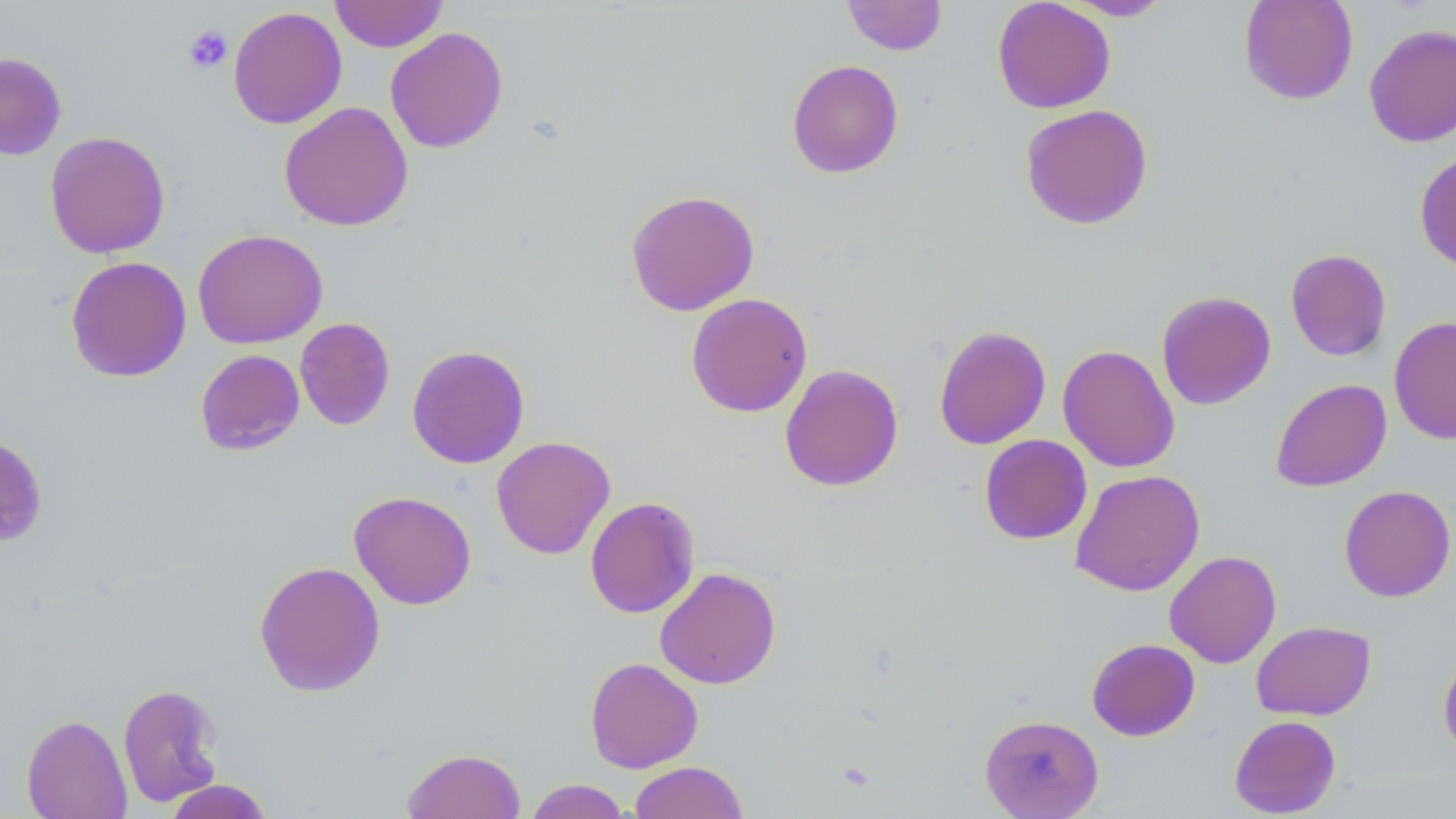

Approximate bounding boxes as named x1/y1/x2/y2 corners in pixels. Uninfected red blood cell locations: (x1=330, y1=0, x2=448, y2=52), (x1=842, y1=0, x2=947, y2=56), (x1=992, y1=0, x2=1115, y2=114), (x1=1062, y1=0, x2=1173, y2=21), (x1=1238, y1=0, x2=1359, y2=105), (x1=228, y1=6, x2=346, y2=130), (x1=1364, y1=23, x2=1456, y2=147), (x1=385, y1=27, x2=509, y2=154), (x1=0, y1=51, x2=66, y2=161), (x1=786, y1=59, x2=904, y2=179), (x1=279, y1=101, x2=413, y2=232), (x1=1020, y1=104, x2=1154, y2=230), (x1=45, y1=131, x2=170, y2=258), (x1=1414, y1=150, x2=1456, y2=272), (x1=625, y1=189, x2=760, y2=316), (x1=192, y1=229, x2=328, y2=348), (x1=1279, y1=248, x2=1390, y2=491), (x1=1285, y1=249, x2=1392, y2=361), (x1=65, y1=256, x2=191, y2=382), (x1=1156, y1=290, x2=1276, y2=410), (x1=686, y1=293, x2=813, y2=418), (x1=1389, y1=316, x2=1456, y2=444), (x1=295, y1=317, x2=395, y2=430), (x1=933, y1=324, x2=1051, y2=450), (x1=933, y1=333, x2=1178, y2=454), (x1=1057, y1=344, x2=1180, y2=473), (x1=407, y1=345, x2=530, y2=469), (x1=195, y1=349, x2=305, y2=455), (x1=779, y1=364, x2=904, y2=492), (x1=1270, y1=378, x2=1392, y2=491), (x1=0, y1=432, x2=49, y2=548), (x1=979, y1=434, x2=1091, y2=544), (x1=491, y1=436, x2=616, y2=559), (x1=1070, y1=469, x2=1205, y2=596), (x1=1339, y1=485, x2=1455, y2=602), (x1=349, y1=490, x2=476, y2=610), (x1=584, y1=496, x2=700, y2=618), (x1=1164, y1=550, x2=1282, y2=668), (x1=254, y1=560, x2=385, y2=697), (x1=655, y1=567, x2=781, y2=689), (x1=1251, y1=621, x2=1376, y2=720), (x1=1087, y1=638, x2=1200, y2=741), (x1=1438, y1=651, x2=1456, y2=764), (x1=585, y1=657, x2=703, y2=773), (x1=117, y1=683, x2=224, y2=808), (x1=980, y1=713, x2=1104, y2=818), (x1=21, y1=714, x2=132, y2=818), (x1=1229, y1=715, x2=1342, y2=817), (x1=402, y1=748, x2=525, y2=819), (x1=628, y1=761, x2=748, y2=819), (x1=524, y1=779, x2=632, y2=818), (x1=162, y1=780, x2=274, y2=818). Platelet locations: (x1=183, y1=24, x2=233, y2=74). Slide-level diagnosis: no evidence of blood parasites. Thin blood film. Image is 1456×819 pixels. Single field of view. May-Grünwald-Giemsa stain. Optical microscopy. 1000x magnification.